Give the extent of all white blood cells.
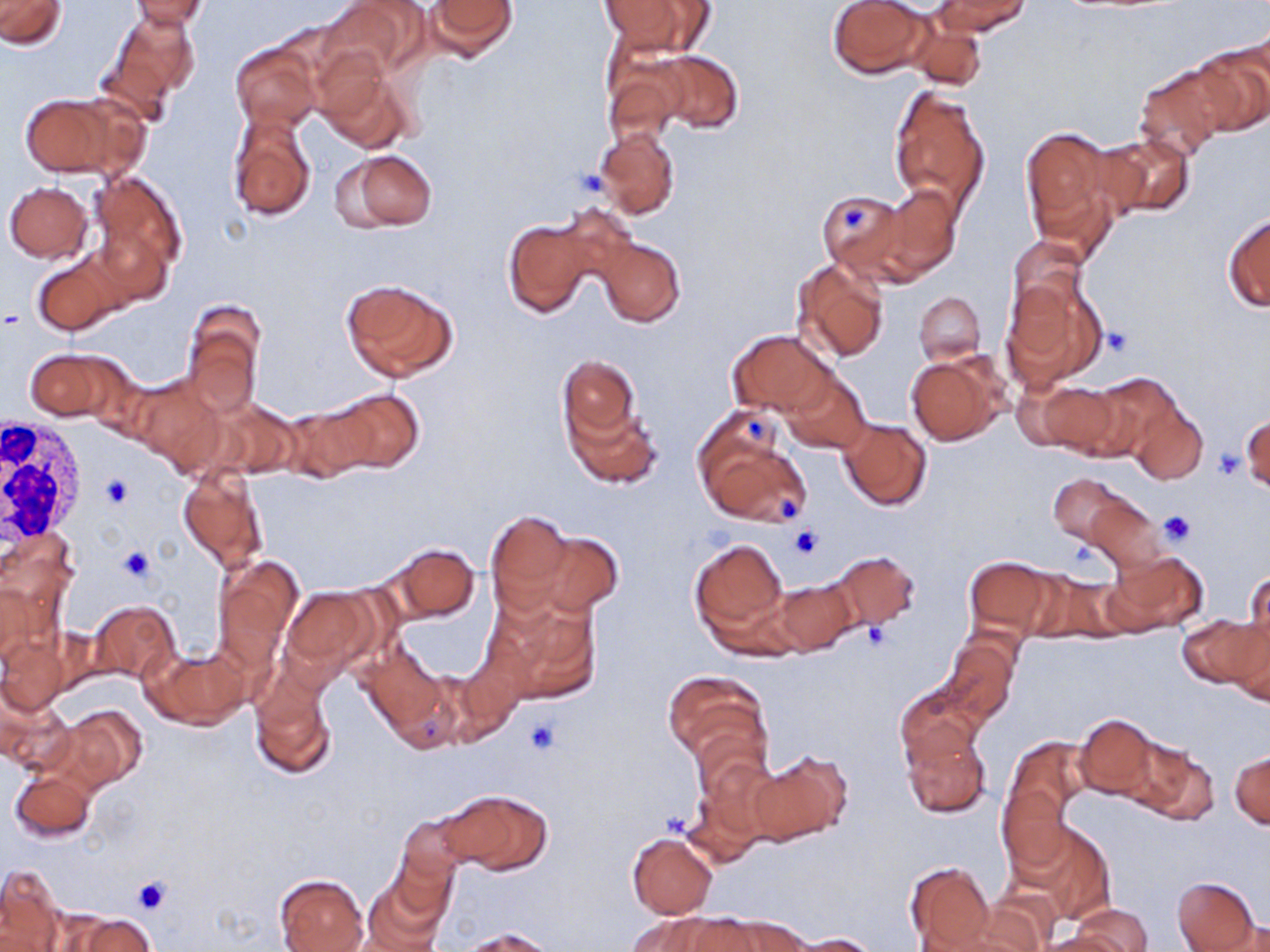
Approximate bounding boxes as [x1, y1, x2, y2] in pixels.
White blood cells: [0, 414, 88, 546].

Summary:
  - Platelet locations: [573, 167, 609, 197], [839, 203, 871, 232], [1104, 328, 1132, 356], [747, 417, 765, 441], [1214, 445, 1242, 480], [102, 476, 130, 509], [777, 495, 801, 521], [1158, 510, 1195, 546], [789, 524, 825, 559], [119, 546, 156, 582], [857, 621, 895, 652], [524, 715, 561, 756], [132, 876, 172, 915]
  - Uninfected red blood cell locations: [0, 0, 67, 47], [126, 0, 212, 29], [320, 0, 427, 83], [425, 0, 518, 61], [827, 0, 933, 78], [932, 0, 1030, 36], [600, 1, 692, 54], [105, 10, 197, 115], [908, 17, 987, 94], [230, 40, 322, 131], [1188, 40, 1269, 135], [654, 51, 744, 134], [601, 57, 685, 148], [315, 59, 414, 152], [1133, 65, 1231, 159], [889, 84, 991, 216], [18, 91, 141, 179], [229, 111, 316, 222], [596, 127, 679, 218], [1020, 127, 1118, 246], [1099, 133, 1194, 219], [341, 149, 438, 230], [87, 169, 187, 286], [4, 181, 93, 263], [877, 183, 962, 281], [815, 188, 907, 278], [1224, 212, 1270, 312], [503, 217, 594, 319], [1006, 235, 1089, 321], [595, 237, 686, 327], [34, 253, 128, 335], [790, 259, 889, 364], [1002, 275, 1107, 390], [341, 279, 458, 384], [915, 292, 985, 365], [181, 303, 265, 418], [727, 330, 835, 418], [26, 348, 121, 421], [556, 353, 643, 448], [906, 355, 1006, 445], [783, 371, 871, 454], [1085, 373, 1182, 459], [133, 376, 226, 471], [1035, 379, 1123, 457], [327, 388, 423, 476], [216, 399, 304, 480], [564, 401, 661, 488], [1130, 402, 1207, 485], [278, 403, 377, 482], [1242, 413, 1268, 493], [839, 419, 932, 511], [696, 420, 811, 528], [178, 467, 269, 576], [1050, 473, 1130, 546], [1086, 498, 1165, 573], [485, 509, 577, 612], [531, 531, 623, 617], [688, 535, 790, 641], [387, 543, 479, 622], [825, 550, 917, 627], [1107, 551, 1207, 635], [210, 556, 302, 676], [964, 556, 1053, 640], [1021, 569, 1116, 642], [1244, 569, 1269, 657], [771, 579, 857, 656], [0, 580, 43, 669], [281, 588, 374, 672], [486, 589, 602, 705], [87, 600, 180, 683], [1179, 612, 1267, 693], [0, 636, 69, 715], [941, 636, 1019, 727], [146, 645, 250, 729], [359, 646, 449, 741], [663, 670, 769, 766], [250, 674, 337, 780], [893, 683, 986, 769], [1, 694, 76, 776], [52, 704, 146, 794], [1074, 714, 1160, 799], [901, 725, 993, 820], [1122, 737, 1219, 826], [999, 738, 1085, 872], [748, 752, 851, 844], [1230, 752, 1269, 829], [9, 767, 96, 842], [442, 788, 552, 873], [680, 789, 765, 868], [397, 814, 468, 889], [1022, 823, 1115, 925], [626, 832, 717, 919], [905, 860, 996, 949], [0, 865, 66, 951], [360, 869, 450, 952], [275, 874, 368, 952], [1171, 875, 1260, 951], [945, 903, 1049, 952], [1071, 904, 1152, 951], [64, 912, 153, 952], [629, 912, 731, 952], [702, 913, 810, 952], [1212, 921, 1270, 952], [455, 928, 556, 951], [786, 932, 881, 951], [1040, 932, 1129, 952]
  - Slide-level diagnosis: no evidence of blood parasites
  - Stain: May-Grünwald-Giemsa
  - Preparation: thin blood film
  - Modality: light microscopy
  - Field of view: single
  - Image size: 1270×952 pixels
  - Magnification: 1000x